Classify this cell by malaria status.
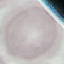

It is uninfected.

capture = smartphone through the microscope eyepiece
stain = Giemsa
image type = cell patch, automatically extracted from a larger field of view and resized to 64 × 64 pixels
preparation = thin blood film